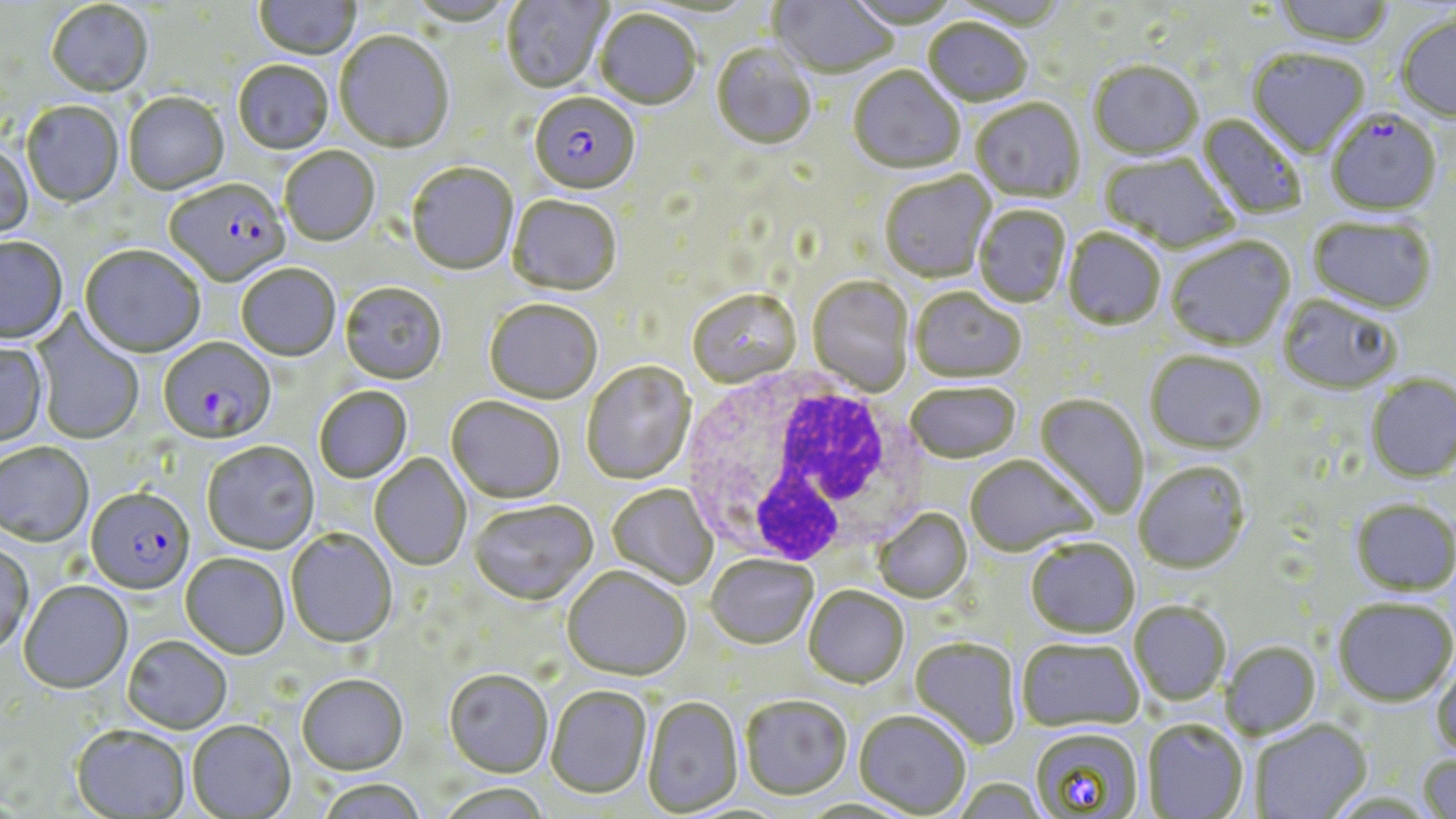
slide-level diagnosis = Plasmodium falciparum
uninfected red blood cell locations = approximate bounding boxes as (x1, y1, x2, y2) in pixels: (253, 0, 362, 61), (502, 0, 612, 94), (770, 0, 898, 79), (1271, 0, 1396, 49), (404, 1, 517, 27), (844, 1, 961, 31), (944, 1, 1068, 31), (46, 2, 154, 99), (595, 11, 702, 111), (1395, 13, 1456, 123), (923, 20, 1032, 108), (335, 32, 454, 156), (711, 45, 816, 151), (1247, 49, 1371, 160), (233, 62, 334, 156), (1089, 64, 1203, 162), (848, 67, 964, 175), (123, 94, 229, 196), (971, 100, 1085, 204), (21, 101, 124, 208), (1197, 113, 1306, 220), (0, 143, 33, 242), (280, 148, 380, 248), (1099, 154, 1237, 255), (406, 165, 517, 276), (880, 172, 997, 285), (508, 197, 622, 297), (973, 206, 1071, 309), (1308, 217, 1437, 315), (1063, 230, 1165, 332), (1166, 237, 1295, 352), (0, 238, 68, 346), (79, 247, 205, 359), (236, 265, 340, 362), (808, 278, 914, 396), (340, 284, 447, 386), (910, 289, 1026, 385), (688, 291, 800, 389), (1277, 295, 1402, 395), (484, 301, 603, 406), (30, 310, 145, 446), (0, 341, 48, 448), (1145, 352, 1266, 455), (582, 362, 696, 486), (1366, 374, 1456, 483), (906, 385, 1020, 465), (314, 387, 413, 484), (1033, 394, 1147, 519), (446, 398, 566, 505), (201, 443, 320, 555), (0, 444, 94, 548), (370, 454, 471, 571), (965, 456, 1096, 558), (1135, 462, 1251, 575), (607, 485, 717, 589), (1350, 498, 1455, 596), (469, 501, 598, 608), (874, 510, 973, 604), (286, 530, 397, 649), (1026, 540, 1139, 639), (0, 544, 34, 657), (180, 554, 290, 660), (706, 556, 818, 650), (561, 567, 692, 683), (19, 582, 133, 695), (803, 587, 909, 689), (1332, 598, 1456, 707), (1129, 601, 1231, 706), (123, 636, 232, 735), (910, 638, 1021, 751), (1017, 639, 1143, 732), (1221, 641, 1321, 739), (1431, 659, 1456, 760), (444, 670, 553, 778), (297, 675, 408, 776), (546, 686, 651, 799), (740, 696, 852, 801), (642, 697, 744, 817), (854, 711, 971, 817), (1251, 719, 1372, 819), (1142, 720, 1248, 819), (187, 721, 296, 818), (71, 725, 189, 818), (1029, 728, 1144, 817), (1416, 752, 1456, 819), (953, 778, 1047, 819), (315, 779, 428, 819), (434, 784, 554, 819), (795, 798, 918, 819)
image size = 1456×819 pixels
field of view = single
magnification = 1000x
stain = May-Grünwald-Giemsa
modality = optical microscopy
white blood cell locations = approximate bounding boxes as (x1, y1, x2, y2) in pixels: (678, 369, 927, 571)
Plasmodium falciparum-infected red blood cell locations = approximate bounding boxes as (x1, y1, x2, y2) in pixels: (529, 95, 641, 197), (1326, 111, 1443, 217), (161, 180, 286, 287), (158, 339, 275, 446), (86, 489, 195, 596)
preparation = thin blood film